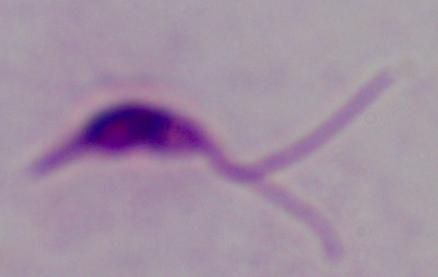

identification = Leishmania
magnification = 1000x
modality = micrograph